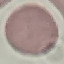

result = no malaria parasites seen
stain = Giemsa
image type = cell patch, automatically extracted from a larger field of view and resized to 64 × 64 pixels
preparation = thin blood smear
capture = smartphone camera at the microscope eyepiece